Identify the blood parasite species.
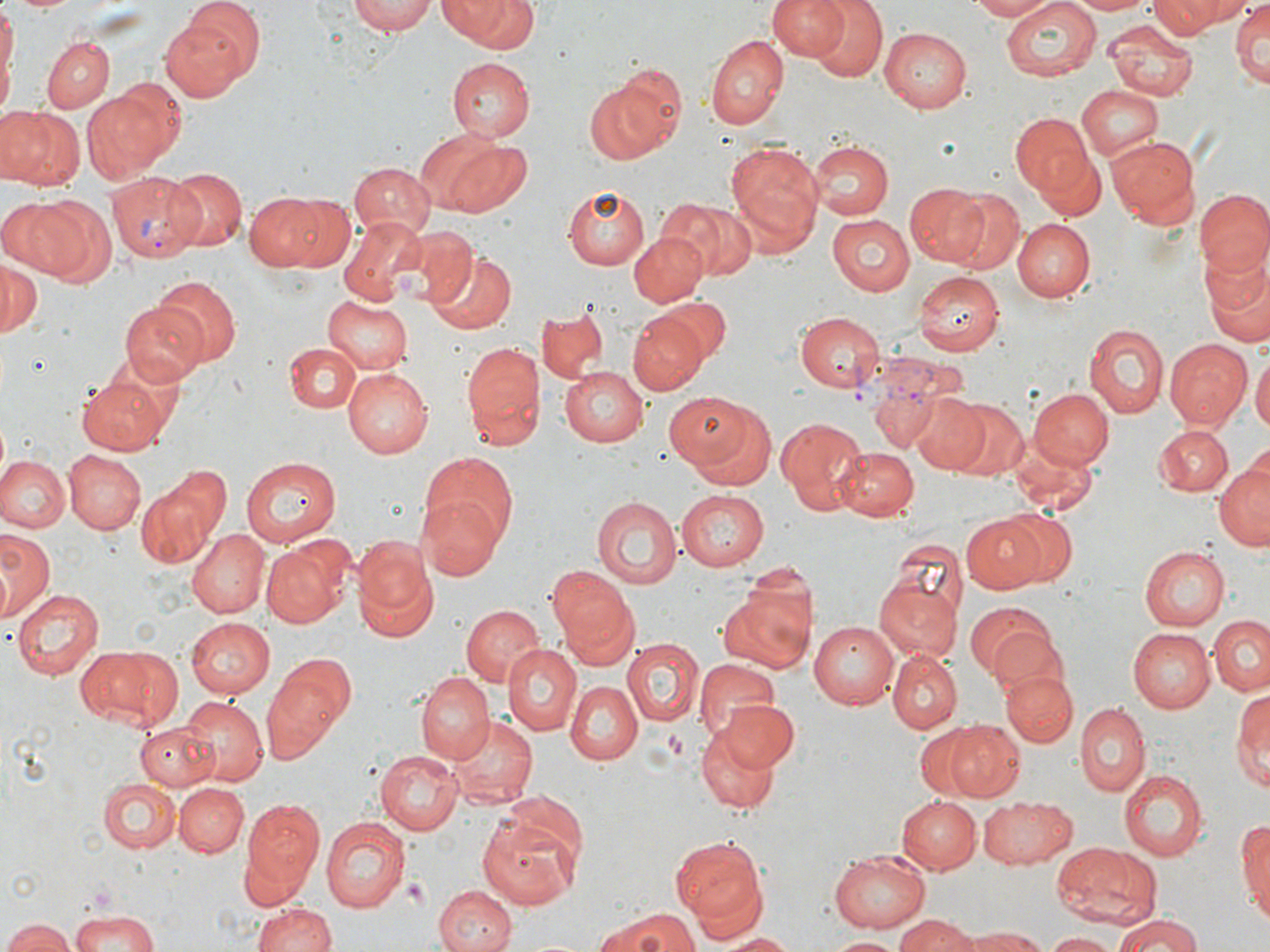
Plasmodium vivax.

Approximate bounding boxes as named x1/y1/x2/y2 corners in pixels. Uninfected red blood cell locations: (x1=1, y1=0, x2=16, y2=113), (x1=10, y1=0, x2=80, y2=14), (x1=348, y1=0, x2=436, y2=35), (x1=440, y1=0, x2=539, y2=53), (x1=767, y1=0, x2=851, y2=60), (x1=805, y1=0, x2=889, y2=82), (x1=965, y1=0, x2=1057, y2=21), (x1=998, y1=0, x2=1103, y2=83), (x1=1064, y1=0, x2=1153, y2=15), (x1=1147, y1=0, x2=1229, y2=39), (x1=1166, y1=0, x2=1258, y2=27), (x1=1230, y1=0, x2=1269, y2=89), (x1=161, y1=9, x2=255, y2=99), (x1=1104, y1=19, x2=1197, y2=101), (x1=879, y1=27, x2=972, y2=112), (x1=704, y1=36, x2=788, y2=131), (x1=42, y1=37, x2=114, y2=113), (x1=448, y1=57, x2=535, y2=141), (x1=615, y1=63, x2=686, y2=147), (x1=584, y1=81, x2=679, y2=164), (x1=84, y1=82, x2=179, y2=179), (x1=1075, y1=85, x2=1163, y2=161), (x1=1, y1=106, x2=83, y2=191), (x1=1010, y1=113, x2=1096, y2=200), (x1=420, y1=135, x2=530, y2=220), (x1=1108, y1=135, x2=1199, y2=230), (x1=808, y1=139, x2=894, y2=220), (x1=725, y1=141, x2=826, y2=250), (x1=1031, y1=144, x2=1108, y2=223), (x1=348, y1=163, x2=434, y2=238), (x1=163, y1=167, x2=248, y2=255), (x1=903, y1=181, x2=991, y2=266), (x1=565, y1=185, x2=651, y2=270), (x1=946, y1=189, x2=1025, y2=273), (x1=1196, y1=190, x2=1270, y2=279), (x1=243, y1=191, x2=328, y2=270), (x1=277, y1=195, x2=355, y2=269), (x1=23, y1=196, x2=116, y2=286), (x1=657, y1=196, x2=757, y2=280), (x1=0, y1=198, x2=73, y2=273), (x1=827, y1=214, x2=916, y2=297), (x1=339, y1=217, x2=427, y2=305), (x1=1011, y1=218, x2=1095, y2=302), (x1=398, y1=226, x2=476, y2=309), (x1=629, y1=233, x2=707, y2=306), (x1=1197, y1=246, x2=1270, y2=348), (x1=426, y1=250, x2=516, y2=333), (x1=0, y1=260, x2=42, y2=339), (x1=914, y1=272, x2=1002, y2=353), (x1=152, y1=278, x2=241, y2=367), (x1=656, y1=293, x2=733, y2=362), (x1=322, y1=296, x2=414, y2=373), (x1=120, y1=304, x2=209, y2=385), (x1=536, y1=309, x2=607, y2=384), (x1=795, y1=312, x2=884, y2=393), (x1=627, y1=313, x2=707, y2=394), (x1=1085, y1=322, x2=1169, y2=421), (x1=1165, y1=338, x2=1252, y2=430), (x1=460, y1=339, x2=544, y2=447), (x1=284, y1=340, x2=362, y2=412), (x1=1251, y1=352, x2=1269, y2=441), (x1=560, y1=365, x2=651, y2=447), (x1=343, y1=367, x2=431, y2=457), (x1=78, y1=374, x2=174, y2=454), (x1=868, y1=379, x2=948, y2=455), (x1=1029, y1=388, x2=1112, y2=470), (x1=907, y1=392, x2=988, y2=473), (x1=671, y1=393, x2=778, y2=488), (x1=944, y1=397, x2=1027, y2=481), (x1=775, y1=418, x2=866, y2=516), (x1=1156, y1=426, x2=1233, y2=497), (x1=1005, y1=436, x2=1099, y2=519), (x1=836, y1=447, x2=919, y2=519), (x1=62, y1=450, x2=144, y2=534), (x1=419, y1=450, x2=519, y2=549), (x1=2, y1=455, x2=68, y2=532), (x1=241, y1=456, x2=338, y2=548), (x1=1214, y1=457, x2=1270, y2=553), (x1=134, y1=464, x2=230, y2=567), (x1=674, y1=490, x2=769, y2=570), (x1=592, y1=496, x2=684, y2=588), (x1=418, y1=499, x2=504, y2=581), (x1=994, y1=507, x2=1078, y2=589), (x1=962, y1=513, x2=1050, y2=594), (x1=1, y1=527, x2=57, y2=623), (x1=187, y1=527, x2=268, y2=617), (x1=260, y1=535, x2=354, y2=628), (x1=884, y1=537, x2=966, y2=628), (x1=352, y1=538, x2=437, y2=641), (x1=1140, y1=546, x2=1227, y2=629), (x1=548, y1=565, x2=639, y2=662), (x1=874, y1=579, x2=961, y2=661), (x1=717, y1=582, x2=814, y2=674), (x1=10, y1=585, x2=104, y2=677), (x1=963, y1=600, x2=1061, y2=686), (x1=459, y1=604, x2=545, y2=689), (x1=1209, y1=615, x2=1270, y2=696), (x1=183, y1=617, x2=274, y2=697), (x1=808, y1=621, x2=901, y2=710), (x1=1128, y1=627, x2=1214, y2=712), (x1=623, y1=638, x2=703, y2=726), (x1=504, y1=644, x2=580, y2=735), (x1=73, y1=645, x2=174, y2=728), (x1=890, y1=650, x2=962, y2=732), (x1=262, y1=652, x2=356, y2=758), (x1=694, y1=659, x2=781, y2=749), (x1=1000, y1=669, x2=1077, y2=746), (x1=416, y1=675, x2=492, y2=766), (x1=567, y1=679, x2=644, y2=765), (x1=1233, y1=684, x2=1269, y2=793), (x1=180, y1=696, x2=267, y2=784), (x1=718, y1=702, x2=799, y2=770), (x1=1074, y1=702, x2=1150, y2=796), (x1=451, y1=716, x2=538, y2=808), (x1=945, y1=720, x2=1027, y2=799), (x1=135, y1=721, x2=219, y2=789), (x1=696, y1=723, x2=784, y2=814), (x1=375, y1=748, x2=463, y2=834), (x1=1120, y1=770, x2=1207, y2=861), (x1=98, y1=779, x2=179, y2=853), (x1=175, y1=782, x2=249, y2=858), (x1=498, y1=791, x2=589, y2=878), (x1=983, y1=794, x2=1076, y2=868), (x1=898, y1=795, x2=981, y2=874), (x1=241, y1=802, x2=324, y2=897), (x1=1237, y1=810, x2=1270, y2=922), (x1=476, y1=814, x2=580, y2=910), (x1=322, y1=815, x2=411, y2=913), (x1=674, y1=836, x2=768, y2=926), (x1=1052, y1=843, x2=1160, y2=928), (x1=829, y1=849, x2=932, y2=932), (x1=433, y1=884, x2=518, y2=952), (x1=251, y1=902, x2=340, y2=952), (x1=593, y1=907, x2=701, y2=952), (x1=69, y1=910, x2=163, y2=952), (x1=1116, y1=911, x2=1204, y2=952), (x1=898, y1=913, x2=977, y2=952), (x1=2, y1=918, x2=76, y2=952), (x1=963, y1=927, x2=1049, y2=952), (x1=1041, y1=931, x2=1122, y2=951), (x1=716, y1=932, x2=797, y2=951), (x1=829, y1=936, x2=905, y2=950). Platelet locations: (x1=404, y1=878, x2=426, y2=904). Plasmodium vivax-infected red blood cell locations: (x1=106, y1=173, x2=202, y2=263), (x1=849, y1=345, x2=968, y2=452). Thin blood film. May-Grünwald-Giemsa-stained preparation. Captured at 1000x magnification. Single field of view. Optical microscopy. Image is 1270×952 pixels.